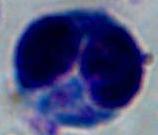
Summary:
  - Identification: leukocyte
  - Modality: micrograph
  - Magnification: 1000x